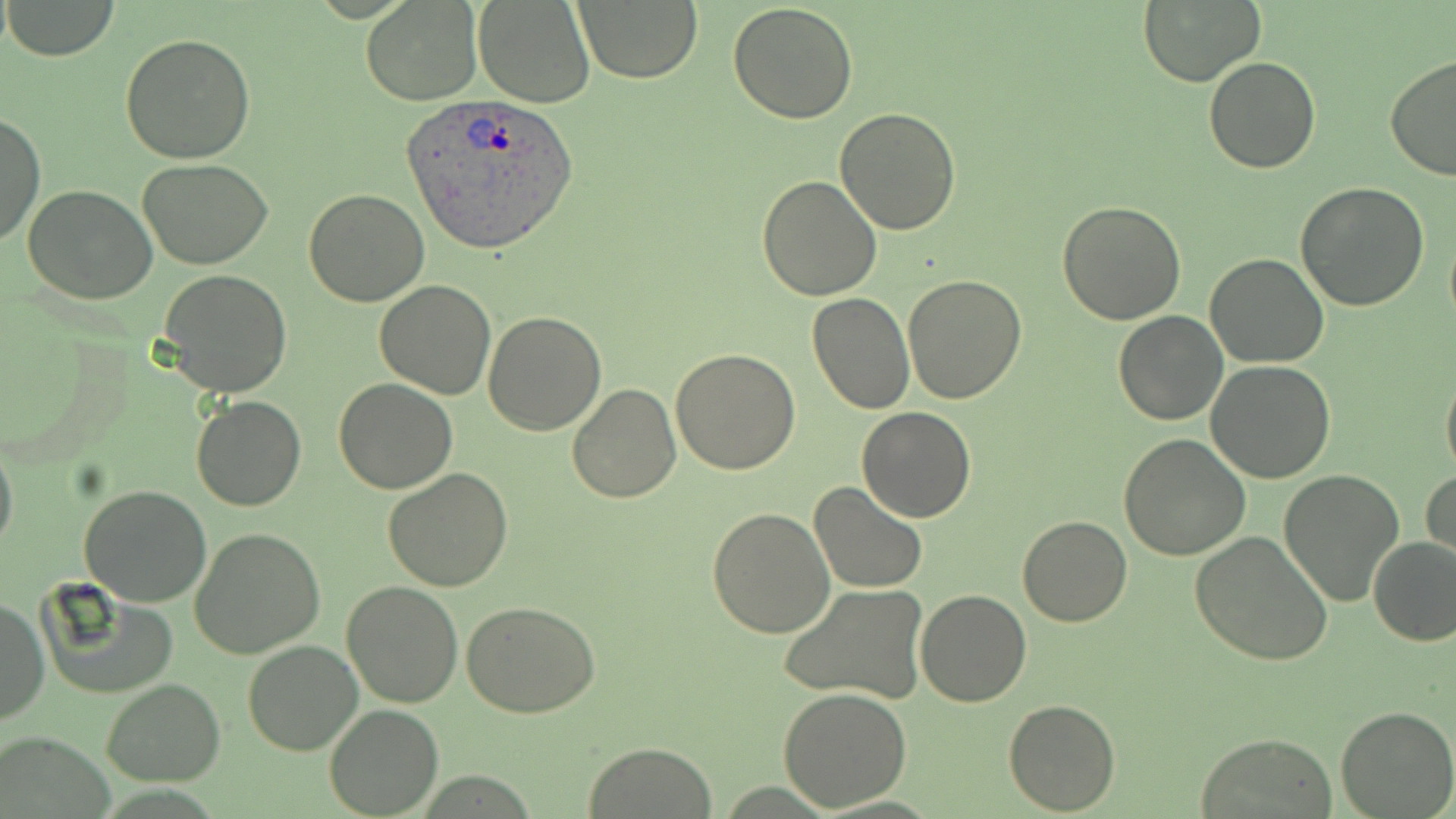
Approximate bounding boxes as [x1, y1, x2, y2] in pixels. Uninfected red blood cell locations: [2, 0, 120, 61], [574, 0, 706, 84], [361, 1, 483, 105], [473, 1, 595, 108], [727, 1, 859, 122], [1137, 2, 1265, 86], [120, 31, 256, 163], [1204, 55, 1321, 174], [1384, 56, 1456, 181], [834, 107, 961, 235], [1, 112, 44, 249], [137, 159, 273, 270], [757, 175, 883, 300], [1295, 182, 1430, 311], [23, 184, 157, 304], [303, 190, 428, 307], [1057, 199, 1186, 324], [1444, 226, 1456, 336], [1205, 252, 1329, 369], [157, 270, 293, 397], [903, 274, 1026, 403], [374, 280, 497, 400], [806, 292, 915, 415], [485, 309, 605, 435], [1114, 310, 1228, 425], [671, 349, 801, 476], [1204, 362, 1335, 483], [1440, 366, 1456, 487], [570, 368, 797, 489], [333, 378, 456, 494], [568, 382, 682, 502], [191, 395, 307, 511], [857, 407, 975, 522], [0, 432, 18, 562], [1119, 433, 1250, 559], [383, 468, 513, 592], [1279, 469, 1405, 607], [1422, 469, 1455, 566], [808, 482, 928, 596], [79, 485, 212, 607], [708, 506, 835, 638], [1017, 514, 1132, 627], [190, 527, 326, 658], [1189, 530, 1334, 665], [1368, 536, 1456, 647], [37, 580, 178, 699], [340, 581, 463, 707], [779, 583, 929, 705], [916, 589, 1032, 707], [1, 595, 48, 725], [461, 601, 601, 718], [242, 637, 364, 756], [101, 678, 224, 786], [777, 686, 913, 811], [1004, 699, 1119, 814], [324, 704, 445, 818], [1336, 706, 1455, 818], [1195, 731, 1338, 818], [583, 741, 717, 818]. Plasmodium ovale-infected red blood cell locations: [401, 94, 580, 253]. Slide-level diagnosis: Plasmodium ovale. May-Grünwald-Giemsa-stained preparation. Image is 1456×819 pixels. Thin blood film. Optical microscopy. Single field of view. Captured at 1000x magnification.